Comment on the morphology of the red blood cells.
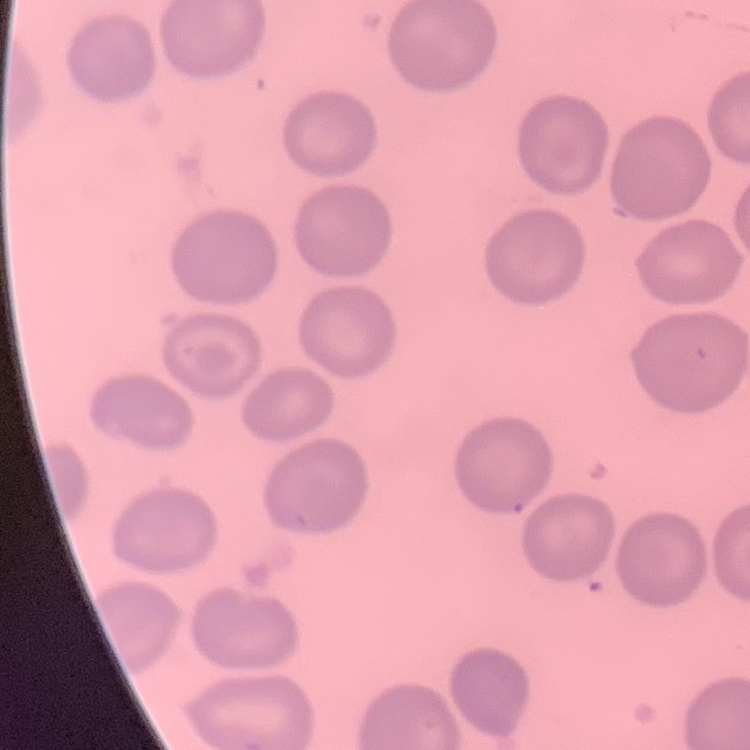
No rouleaux formation.

One tile cut from a larger photomicrograph. Field's or Giemsa stain. Thin peripheral smear.